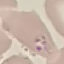

{
  "malaria_status": "parasitized",
  "capture": "smartphone through the microscope eyepiece",
  "stain": "Giemsa",
  "image_type": "automatically extracted cell patch, resized to 64 × 64 pixels",
  "preparation": "thin blood film"
}